Locate every leukocyte (white blood cell).
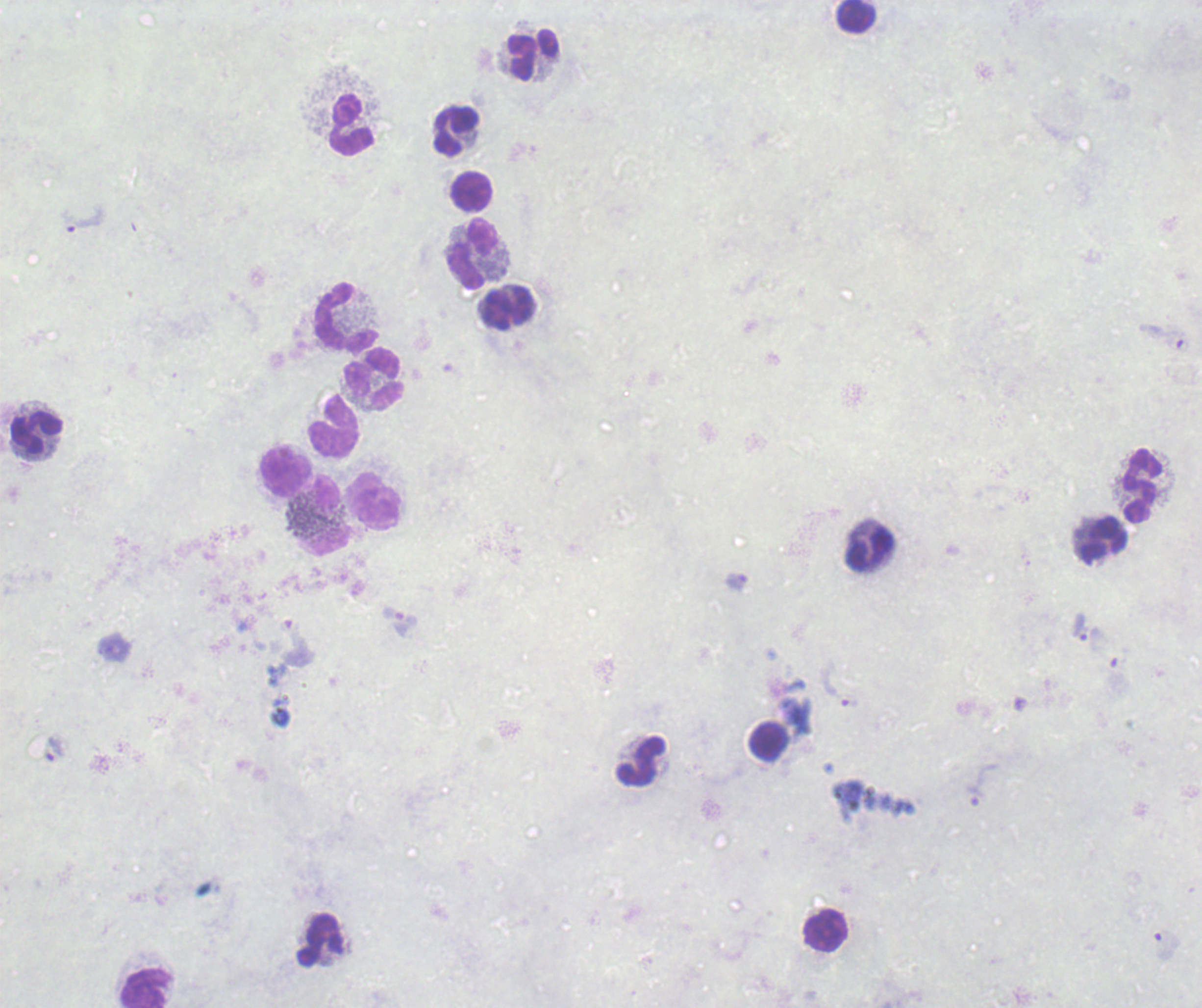
Approximate object centers, in pixels from the top-left corner.
Leukocytes: (x=856, y=16), (x=533, y=55), (x=350, y=125), (x=457, y=130), (x=472, y=191), (x=471, y=254), (x=508, y=308), (x=347, y=316), (x=374, y=378), (x=333, y=425), (x=36, y=432), (x=285, y=471), (x=1143, y=486), (x=374, y=501), (x=326, y=515), (x=1105, y=539), (x=870, y=551), (x=769, y=741), (x=641, y=760), (x=824, y=930), (x=320, y=939), (x=146, y=988).

coordinate format = approximate object centers, in pixels from the top-left corner
trophozoite locations = (x=82, y=218), (x=737, y=581), (x=1080, y=627), (x=841, y=685), (x=55, y=748), (x=984, y=783)
stain = Romanowsky
context = previously used in an actual diagnosis
field of view = single
result = Plasmodium parasites identified
background quality = unsatisfactory
image size = 1202×1008 pixels
magnification = 100x
preparation = thick blood film